Assess the morphology of the erythrocytes.
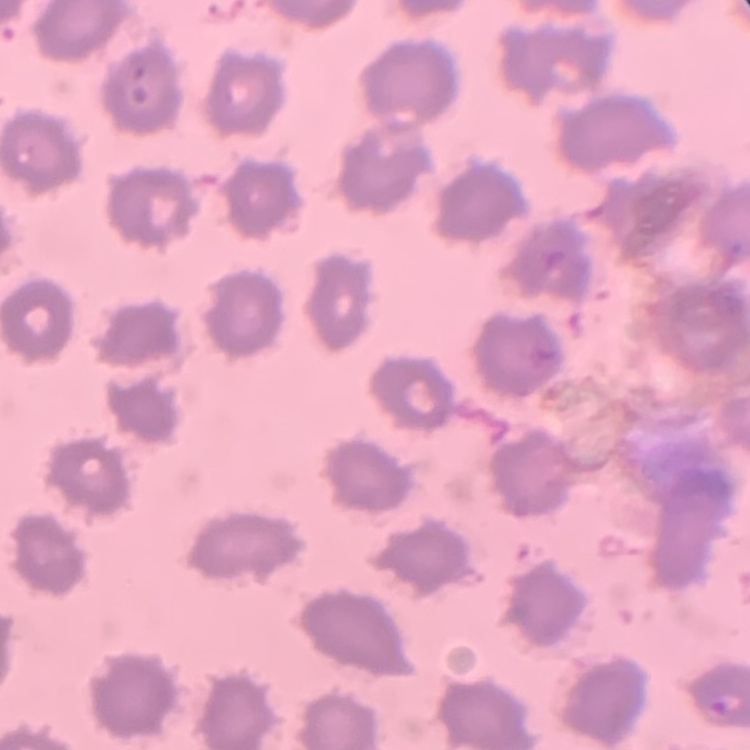

They show no rouleaux formation.

Summary:
  - Preparation: thin blood smear
  - Image type: square crop of a larger photomicrograph
  - Stain: Field's or Giemsa